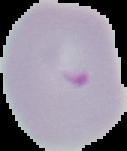

Image is 127×151 pixels. From a thin blood film. Malaria status: parasitized. Segmented cell region on a black background.